Comment on the morphology of the erythrocytes.
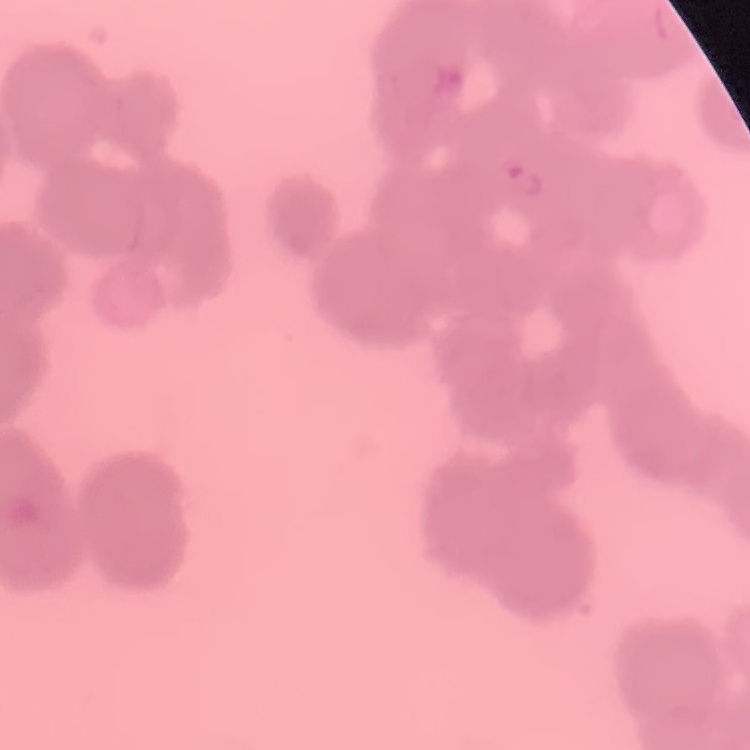
They show rouleaux formation.

stain = Field's or Giemsa
image type = square crop of a larger photomicrograph
preparation = thin blood film